Identify the parasite.
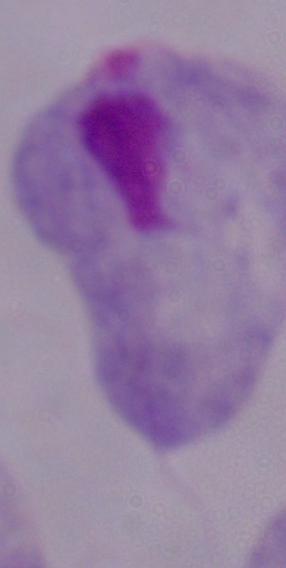

A trichomonad.

{
  "magnification": "1000x",
  "modality": "micrograph"
}